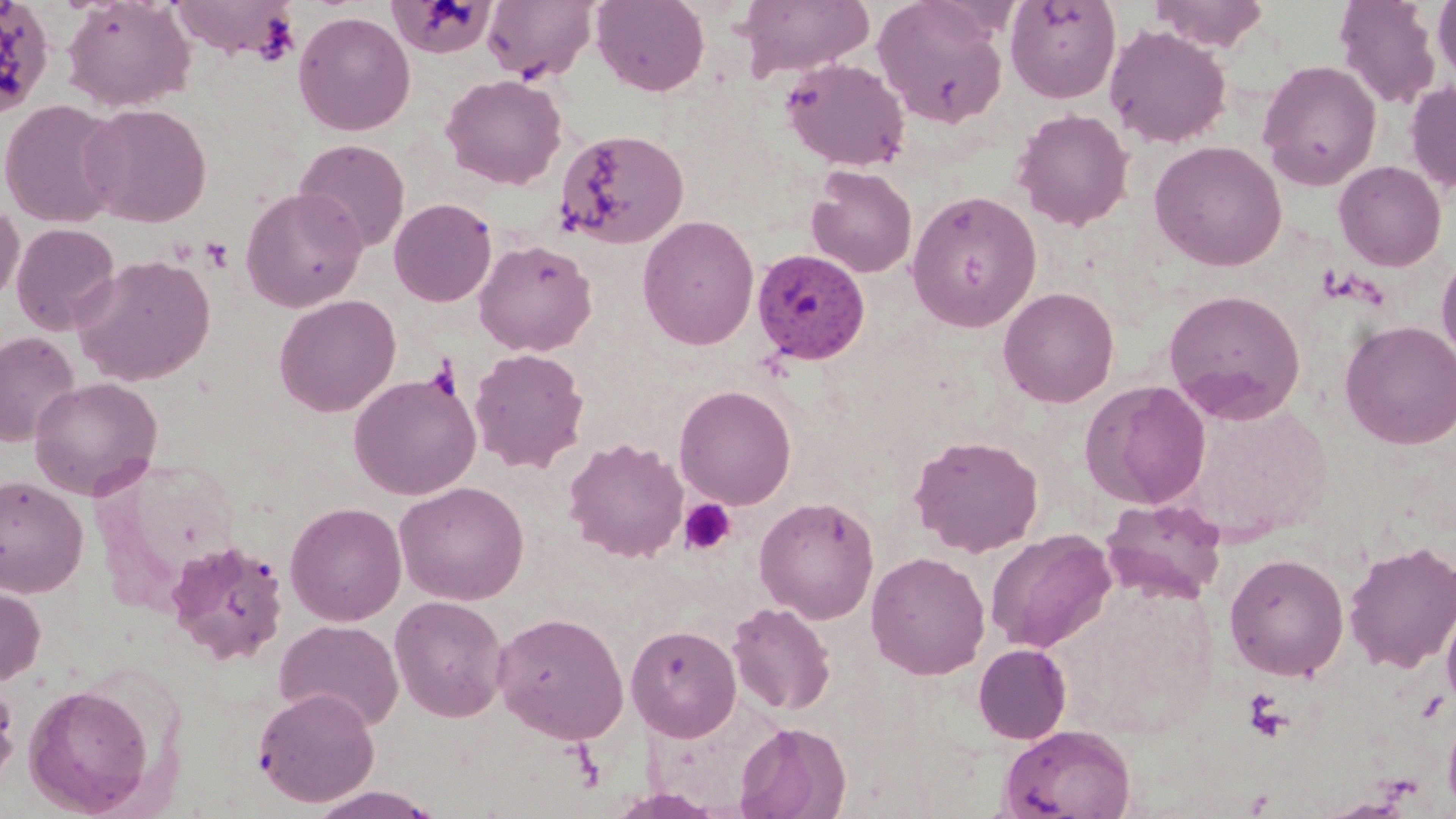
Approximate bounding boxes as (x1, y1, x2, y2) in pixels. Platelet locations: (201, 237, 234, 271), (678, 499, 737, 555), (1242, 690, 1292, 743). Uninfected red blood cell locations: (61, 0, 194, 111), (167, 0, 300, 60), (591, 0, 710, 96), (736, 0, 874, 79), (873, 0, 1010, 129), (1005, 0, 1121, 104), (1147, 0, 1270, 51), (1333, 0, 1442, 110), (388, 1, 498, 59), (481, 1, 598, 83), (1432, 1, 1456, 84), (293, 11, 415, 136), (1104, 24, 1232, 149), (781, 57, 910, 172), (1257, 59, 1382, 189), (440, 73, 567, 190), (1405, 80, 1456, 194), (0, 99, 125, 228), (80, 102, 212, 228), (1013, 108, 1135, 231), (555, 129, 690, 249), (294, 138, 411, 253), (1149, 140, 1287, 271), (1333, 160, 1447, 271), (806, 166, 918, 278), (240, 187, 368, 312), (906, 190, 1043, 332), (389, 198, 497, 307), (0, 200, 24, 306), (637, 215, 759, 350), (11, 222, 120, 335), (474, 238, 597, 357), (1436, 251, 1456, 366), (72, 254, 216, 386), (998, 286, 1119, 408), (1163, 288, 1305, 423), (274, 294, 401, 417), (1339, 319, 1456, 450), (0, 331, 80, 446), (469, 347, 590, 472), (348, 372, 481, 500), (28, 376, 163, 500), (1079, 379, 1211, 510), (674, 384, 797, 509), (1175, 400, 1335, 541), (909, 434, 1044, 557), (563, 437, 688, 562), (0, 475, 89, 598), (394, 480, 530, 605), (754, 496, 879, 623), (1100, 497, 1227, 604), (285, 500, 407, 626), (986, 529, 1116, 653), (166, 538, 290, 665), (1343, 540, 1456, 674), (865, 551, 990, 680), (1224, 552, 1349, 681), (0, 581, 45, 686), (389, 595, 509, 722), (1441, 597, 1456, 713), (727, 601, 836, 716), (492, 610, 629, 744), (274, 619, 404, 730), (626, 624, 742, 742), (973, 643, 1072, 744), (0, 676, 20, 788), (23, 683, 156, 816), (253, 687, 380, 807), (1442, 703, 1456, 815), (735, 720, 851, 819), (998, 724, 1137, 819), (303, 786, 447, 819). Plasmodium malariae-infected red blood cell locations: (751, 248, 871, 365). Slide-level diagnosis: Plasmodium malariae. Captured at 1000x magnification. Single field of view. Image is 1456×819 pixels. May-Grünwald-Giemsa stain. Thin blood film. Optical microscopy.